State which parasite is depicted.
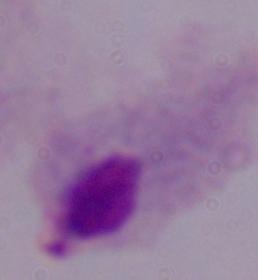

This is a trichomonad.

modality = photomicrograph
magnification = 1000x